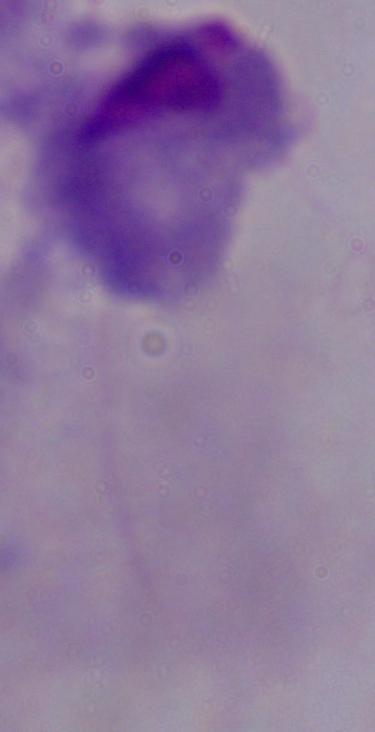
modality: photomicrograph
identification: trichomonad
magnification: 1000x